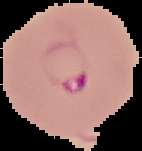 From a thin blood smear. Image is 142×151 pixels. Malaria status: parasitized. Cell region segmented out of the field of view; the surrounding area is masked to black.